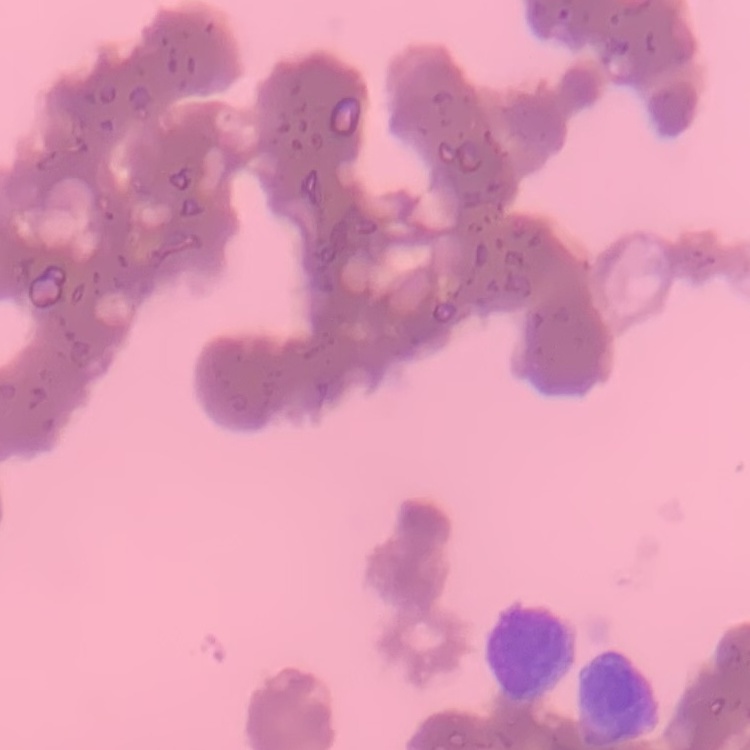 The red blood cells show rouleaux formation. Field's or Giemsa stain. Square crop of a larger photomicrograph. Thin blood smear.